Identify the preparation type.
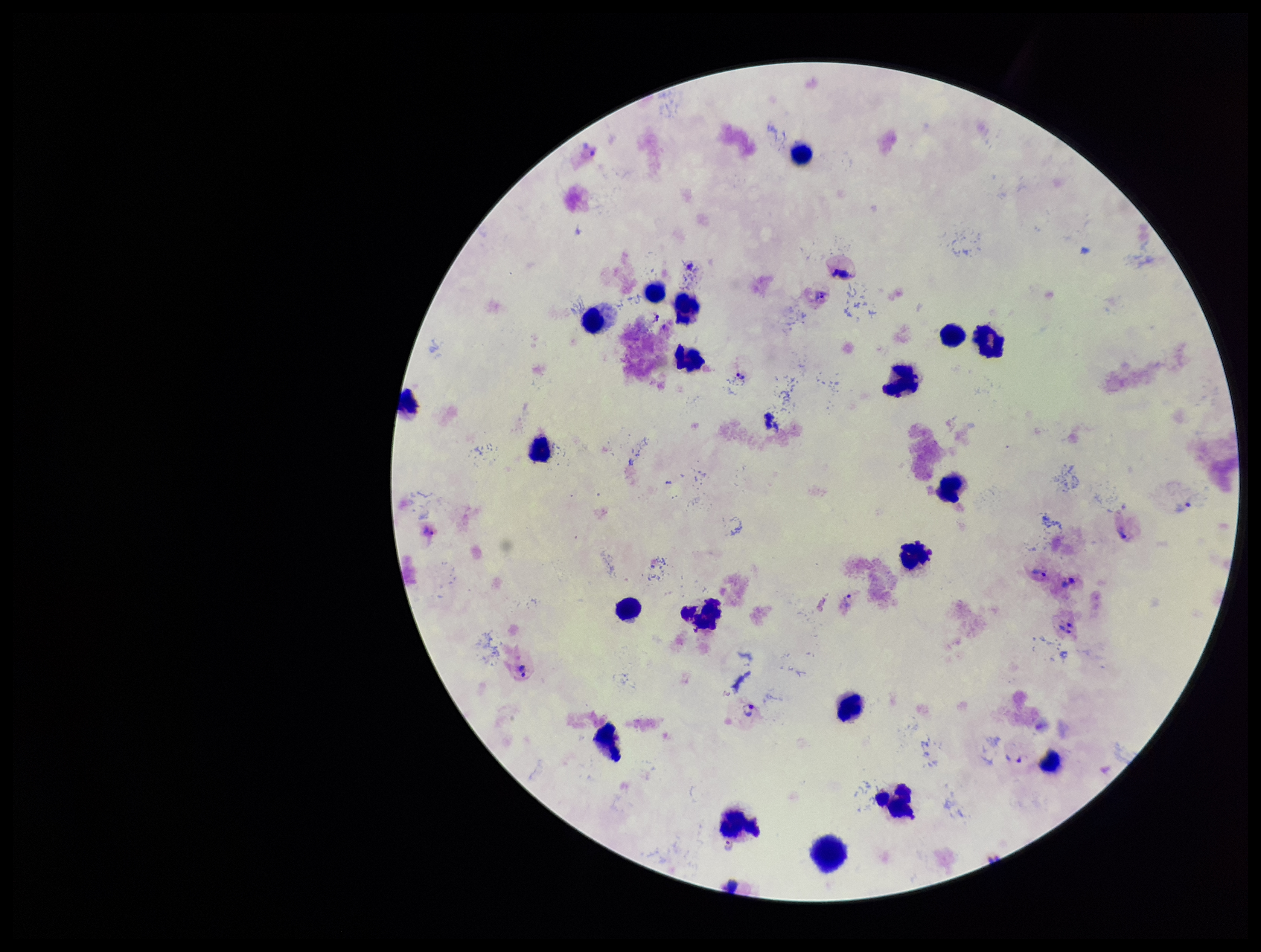

It is a thick blood smear.

capture = smartphone photograph through the microscope eyepiece
field of view = one from this slide
patient malaria status = infected
stain = Giemsa
parasite count = 10
leukocyte count = 19
species reported for this patient = Plasmodium vivax
Plasmodium parasites = identified
image size = 1261×952 pixels